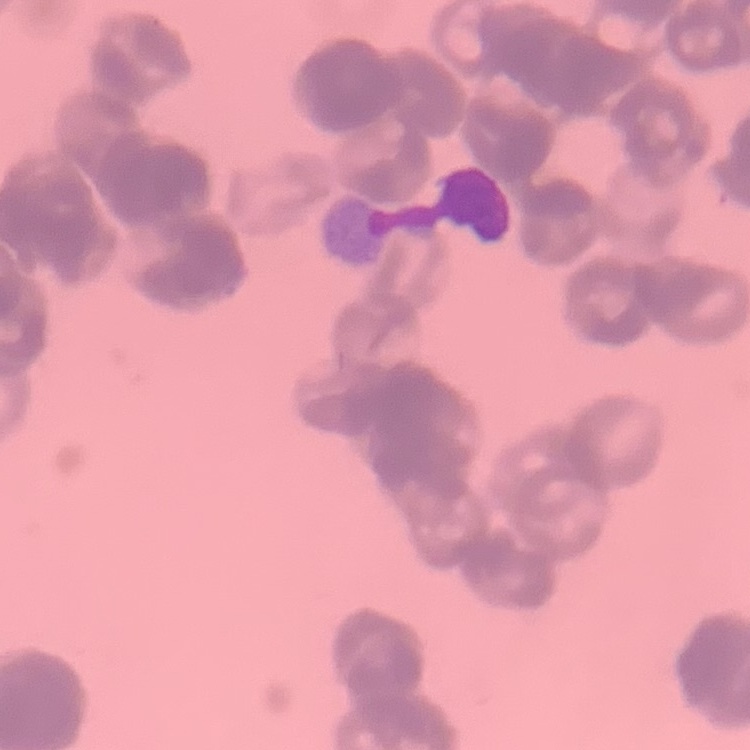

red blood cell morphology = rouleaux formation
preparation = thin blood smear
stain = Field's or Giemsa
image type = one tile cut from a larger photomicrograph